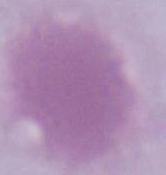
Summary:
  - Magnification: 1000x
  - Identification: erythrocyte
  - Modality: photomicrograph